Identify the cell.
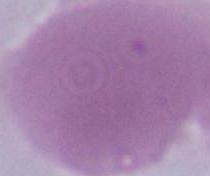
An erythrocyte.

Micrograph. 1000x magnification.